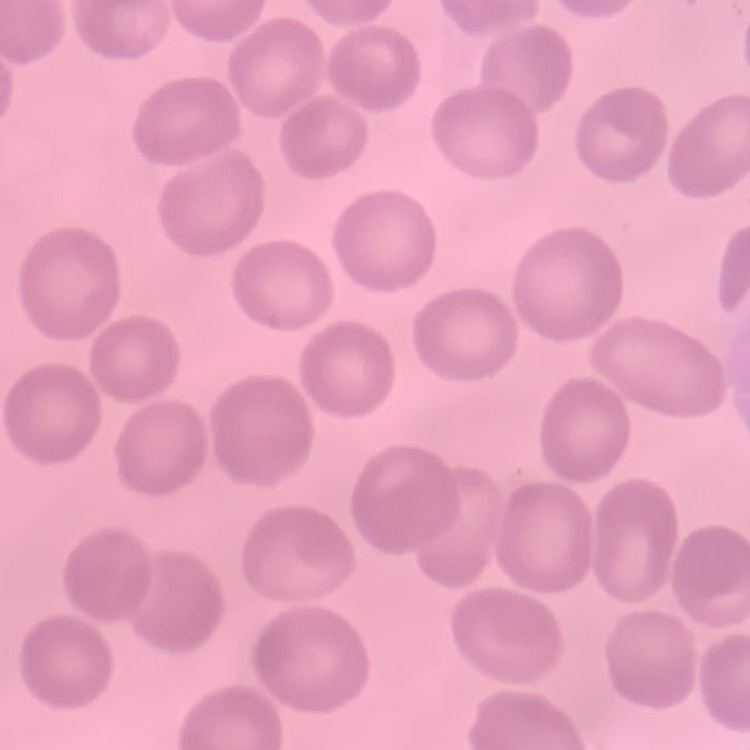
erythrocyte_morphology: no rouleaux formation
preparation: thin blood smear
stain: Field's or Giemsa
image_type: one tile cut from a larger photomicrograph